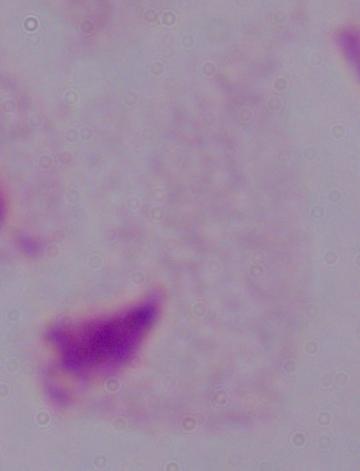

Photomicrograph. A trichomonad is shown. Captured at 1000x magnification.